Name the parasite shown.
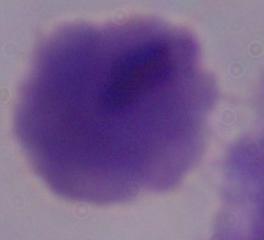

This is a trichomonad.

magnification = 1000x
modality = photomicrograph